Assess this cell for malaria.
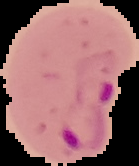

It is parasitized.

Summary:
  - Preparation: thin blood film
  - Image size: 139×166 pixels
  - Image type: segmented cell region on a black background